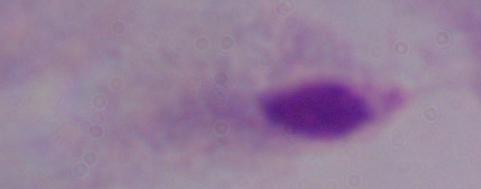

Summary:
  - Modality: micrograph
  - Magnification: 1000x
  - Identification: trichomonad